Name the parasite shown.
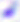

Toxoplasma gondii.

400x magnification. Micrograph.